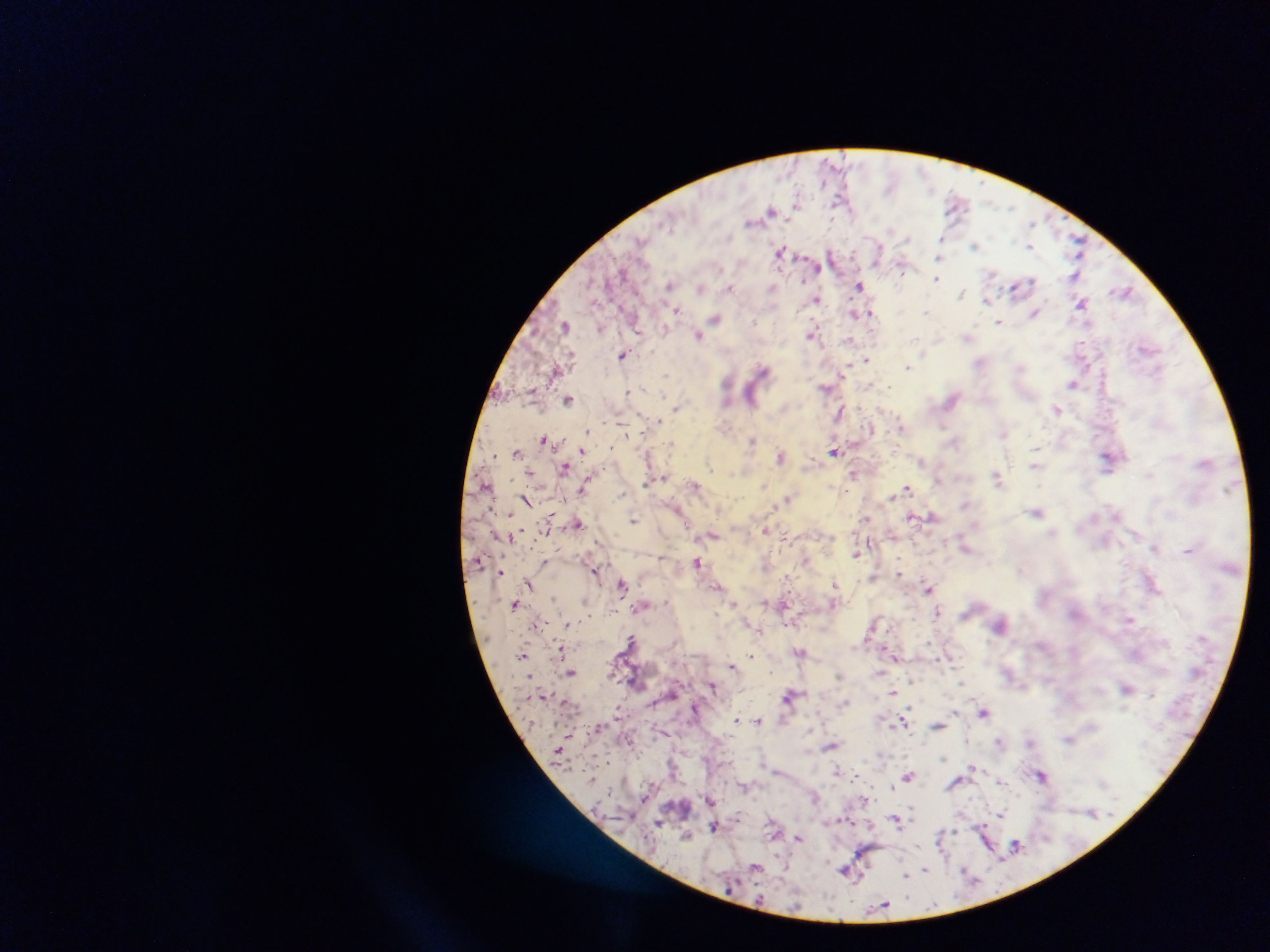

Approximate centers as {x, y} in pixels.
Summary:
  - Plasmodium parasite locations: {796, 202}, {954, 206}, {1010, 207}, {770, 210}, {1032, 223}, {907, 239}, {642, 240}, {941, 240}, {1077, 242}, {976, 245}, {1029, 246}, {779, 251}, {879, 251}, {938, 258}, {817, 267}, {902, 267}, {623, 273}, {992, 274}, {1075, 275}, {937, 279}, {1030, 282}, {669, 286}, {860, 286}, {730, 287}, {1020, 287}, {773, 288}, {701, 289}, {1124, 292}, {962, 294}, {817, 299}, {988, 301}, {1081, 304}, {676, 311}, {927, 312}, {1035, 312}, {856, 313}, {870, 313}, {716, 319}, {999, 322}, {565, 325}, {600, 329}, {636, 329}, {666, 331}, {810, 334}, {698, 335}, {967, 336}, {850, 340}, {1146, 347}, {623, 355}, {865, 358}, {907, 367}, {762, 369}, {845, 370}, {666, 375}, {727, 383}, {1073, 384}, {827, 388}, {628, 392}, {751, 398}, {568, 399}, {677, 407}, {1057, 409}, {839, 413}, {658, 421}, {943, 425}, {901, 427}, {586, 432}, {1003, 433}, {543, 438}, {752, 441}, {1035, 448}, {583, 450}, {834, 451}, {517, 452}, {495, 455}, {780, 456}, {1108, 459}, {921, 461}, {708, 465}, {1034, 465}, {564, 468}, {530, 472}, {855, 473}, {1150, 474}, {997, 477}, {663, 479}, {938, 480}, {694, 486}, {584, 488}, {907, 488}, {845, 490}, {891, 497}, {787, 498}, {525, 500}, {1037, 512}, {510, 514}, {1117, 515}, {932, 516}, {912, 517}, {866, 519}, {634, 520}, {578, 523}, {765, 531}, {891, 535}, {713, 536}, {1155, 548}, {966, 549}, {1188, 551}, {855, 554}, {545, 562}, {697, 563}, {594, 571}, {501, 573}, {899, 573}, {622, 583}, {835, 583}, {529, 585}, {717, 586}, {928, 589}, {554, 599}, {765, 601}, {735, 603}, {833, 603}, {516, 604}, {784, 604}, {938, 612}, {1130, 619}, {568, 623}, {631, 639}, {561, 649}, {800, 652}, {522, 655}, {752, 656}, {896, 656}, {949, 658}, {731, 666}, {571, 672}, {910, 680}, {962, 682}, {712, 686}, {1127, 687}, {894, 693}, {1152, 695}, {790, 696}, {843, 703}, {983, 712}, {736, 719}, {759, 721}, {903, 722}, {937, 726}, {1069, 739}, {966, 740}, {999, 741}, {1031, 741}, {831, 745}, {944, 758}, {972, 767}, {838, 770}, {1042, 775}, {909, 776}, {1001, 782}, {743, 786}, {892, 788}, {815, 796}, {709, 799}, {1001, 814}, {896, 820}, {659, 824}, {714, 826}, {687, 835}, {799, 838}, {1016, 844}, {784, 865}, {755, 866}, {845, 870}, {925, 870}, {965, 871}, {906, 876}, {882, 905}
  - Field of view: single
  - Preparation: thick blood smear
  - Country: Ghana
  - Capture: mobile-phone photograph through a microscope
  - Image size: 1270×952 pixels